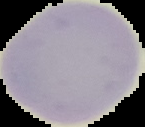
Summary:
  - Image size: 145×127 pixels
  - Result: no Plasmodium parasites seen
  - Image type: cell region segmented out of the field of view; surrounding area masked to black
  - Preparation: thin blood film